Classify this cell by malaria status.
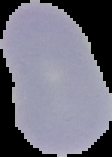

Uninfected.

image size = 112×157 pixels
preparation = thin blood smear
image type = segmented cell region with the area outside set to black